Identify the parasite.
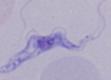
A trypanosome.

Photomicrograph. 1000x magnification.